State which cell type is depicted.
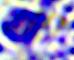
This is a leukocyte.

modality = micrograph
magnification = 400x